Name the parasite shown.
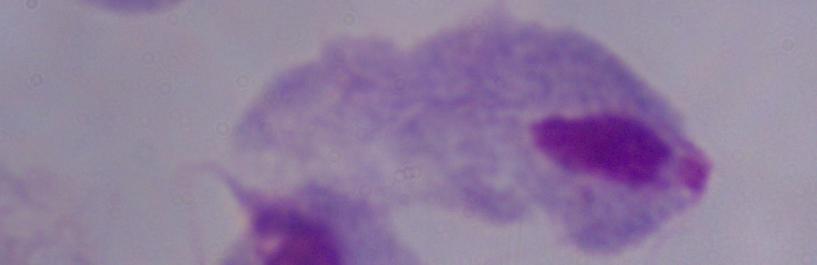
This is a trichomonad.

{
  "modality": "photomicrograph",
  "magnification": "1000x"
}